Locate every Plasmodium falciparum parasite and identify its life-cycle stage.
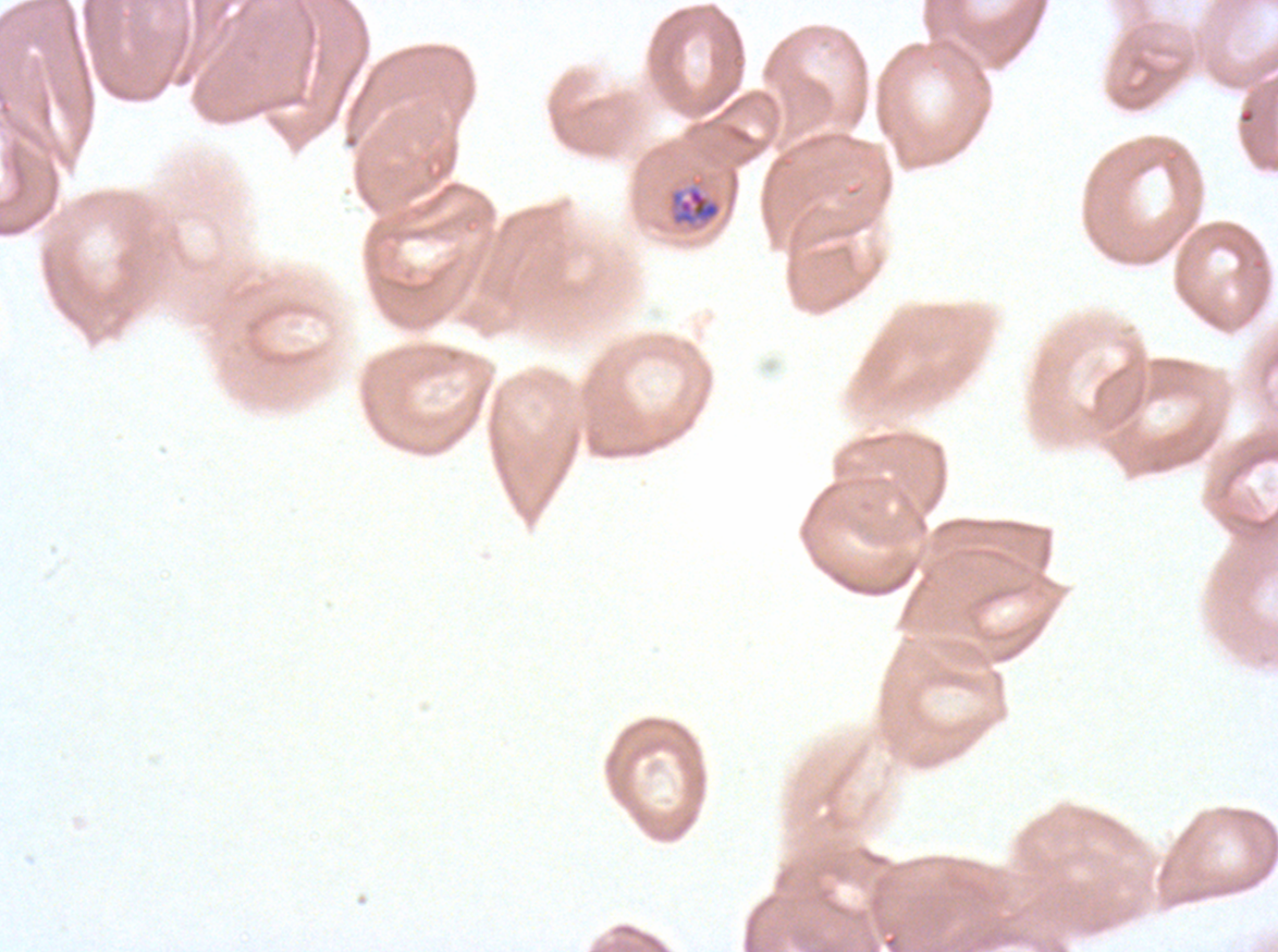

Approximate bounding boxes as (x1, y1, x2, y2) in pixels.
Late-ring/early-trophozoite forms: (670, 186, 721, 226).
No rings, mid trophozoites, late trophozoites, early schizonts, late schizonts, segmenters, or gametocytes observed.

Summary:
  - Preparation: thin blood smear
  - Field of view: one sub-image of a larger composite
  - Specimen: Plasmodium falciparum cultured ex vivo for 24 to 48 hours, from a patient in The Gambia
  - Image size: 1278×952 pixels
  - Stain: Giemsa